State the blood parasite species.
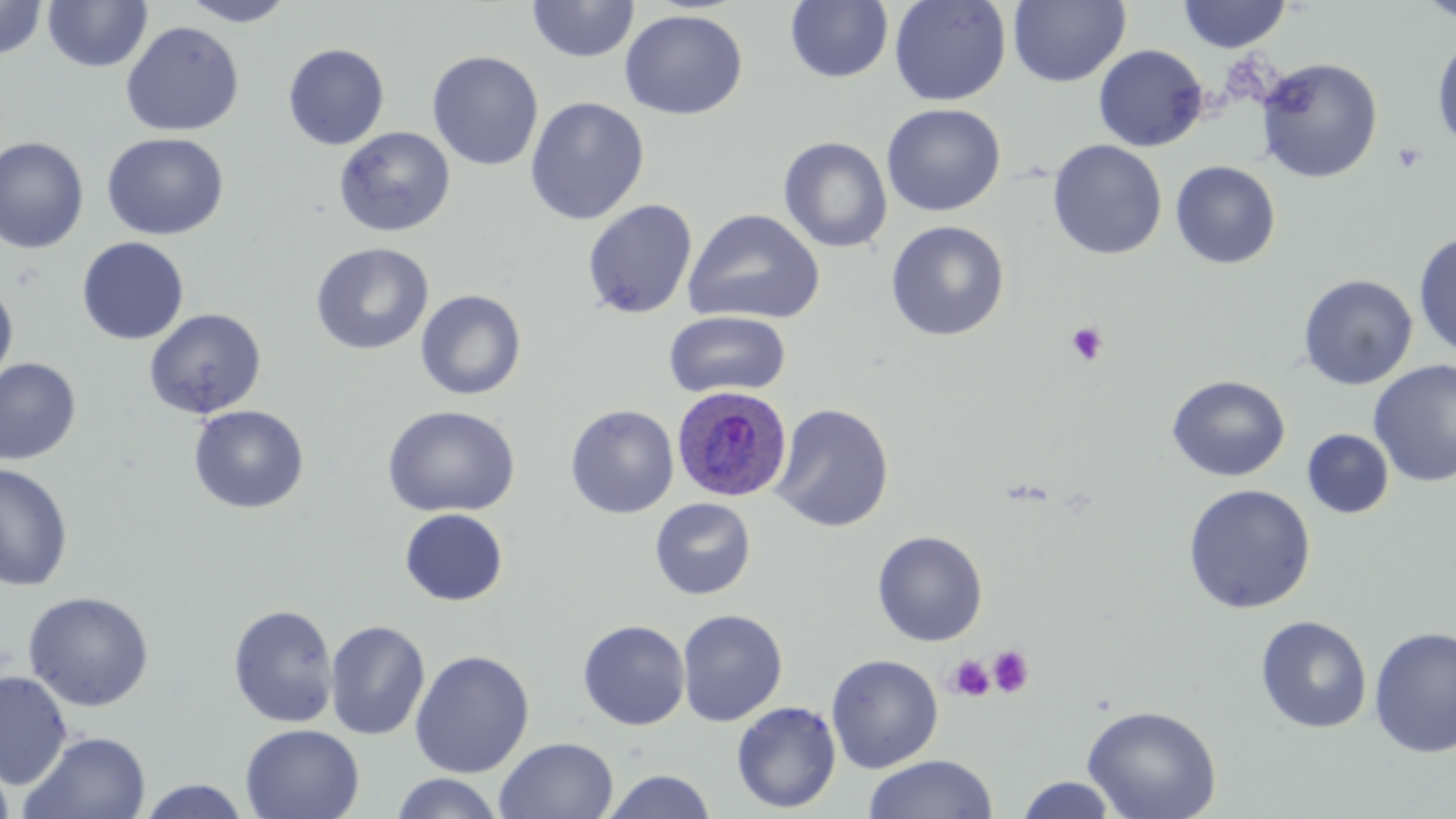

Plasmodium ovale.

field of view = one of a larger specimen
preparation = thin blood film
magnification = 1000x
platelet locations = approximate bounding boxes as (x1, y1, x2, y2) in pixels: (1392, 143, 1426, 172), (1066, 321, 1109, 367), (987, 645, 1035, 697), (946, 654, 994, 701)
stain = May-Grünwald-Giemsa
Plasmodium ovale-infected red blood cell locations = approximate bounding boxes as (x1, y1, x2, y2) in pixels: (671, 385, 793, 503)
image size = 1456×819 pixels
uninfected red blood cell locations = approximate bounding boxes as (x1, y1, x2, y2) in pixels: (0, 0, 49, 61), (179, 0, 296, 27), (527, 0, 639, 63), (889, 0, 1012, 106), (1008, 0, 1130, 87), (1415, 0, 1456, 23), (42, 1, 152, 73), (785, 1, 893, 83), (1177, 1, 1292, 53), (619, 9, 748, 120), (121, 20, 244, 137), (1432, 34, 1456, 153), (283, 43, 390, 150), (1093, 44, 1209, 151), (427, 50, 544, 171), (1256, 57, 1383, 183), (525, 97, 650, 225), (881, 103, 1006, 216), (334, 126, 455, 237), (101, 132, 228, 240), (0, 136, 89, 253), (778, 136, 893, 253), (1047, 139, 1167, 260), (1170, 161, 1281, 269), (581, 199, 698, 319), (683, 208, 826, 326), (885, 220, 1010, 341), (1413, 230, 1456, 359), (77, 237, 189, 345), (310, 242, 433, 356), (1298, 274, 1418, 390), (0, 281, 18, 387), (415, 289, 527, 400), (144, 308, 267, 419), (663, 310, 791, 399), (0, 357, 82, 466), (1369, 361, 1456, 486), (1167, 375, 1290, 482), (770, 403, 895, 532), (565, 404, 679, 519), (188, 405, 309, 514), (382, 405, 520, 518), (1302, 429, 1394, 518), (0, 462, 74, 591), (1182, 483, 1316, 614), (650, 497, 756, 600), (399, 508, 508, 606), (872, 530, 988, 646), (22, 591, 154, 711), (227, 604, 339, 728), (677, 609, 788, 726), (1256, 615, 1373, 734), (325, 619, 430, 740), (577, 620, 691, 730), (1368, 626, 1456, 759), (410, 650, 535, 778), (826, 654, 944, 773), (0, 670, 73, 789), (731, 701, 841, 813), (1082, 704, 1222, 819), (240, 723, 365, 819), (20, 731, 152, 819), (494, 736, 618, 819), (864, 754, 998, 819), (0, 757, 15, 819), (602, 769, 717, 819), (389, 772, 505, 819), (1014, 775, 1120, 818), (135, 778, 252, 818)
modality = optical microscopy